Report the malaria status of this cell.
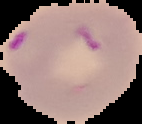

Parasitized.

Summary:
  - Image size: 142×124 pixels
  - Preparation: thin blood film
  - Image type: segmented cell region on a black background